Classify this cell by malaria status.
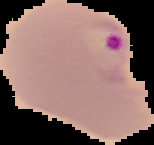

Parasitized.

From a thin blood film. Image is 154×145 pixels. The area outside the segmented cell region is set to black.